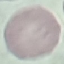
Summary:
  - Malaria status: uninfected
  - Image type: cell patch, automatically extracted from a larger field of view and resized to 64 × 64 pixels
  - Capture: smartphone camera at the microscope eyepiece
  - Preparation: thin blood smear
  - Stain: Giemsa